Locate every malaria parasite.
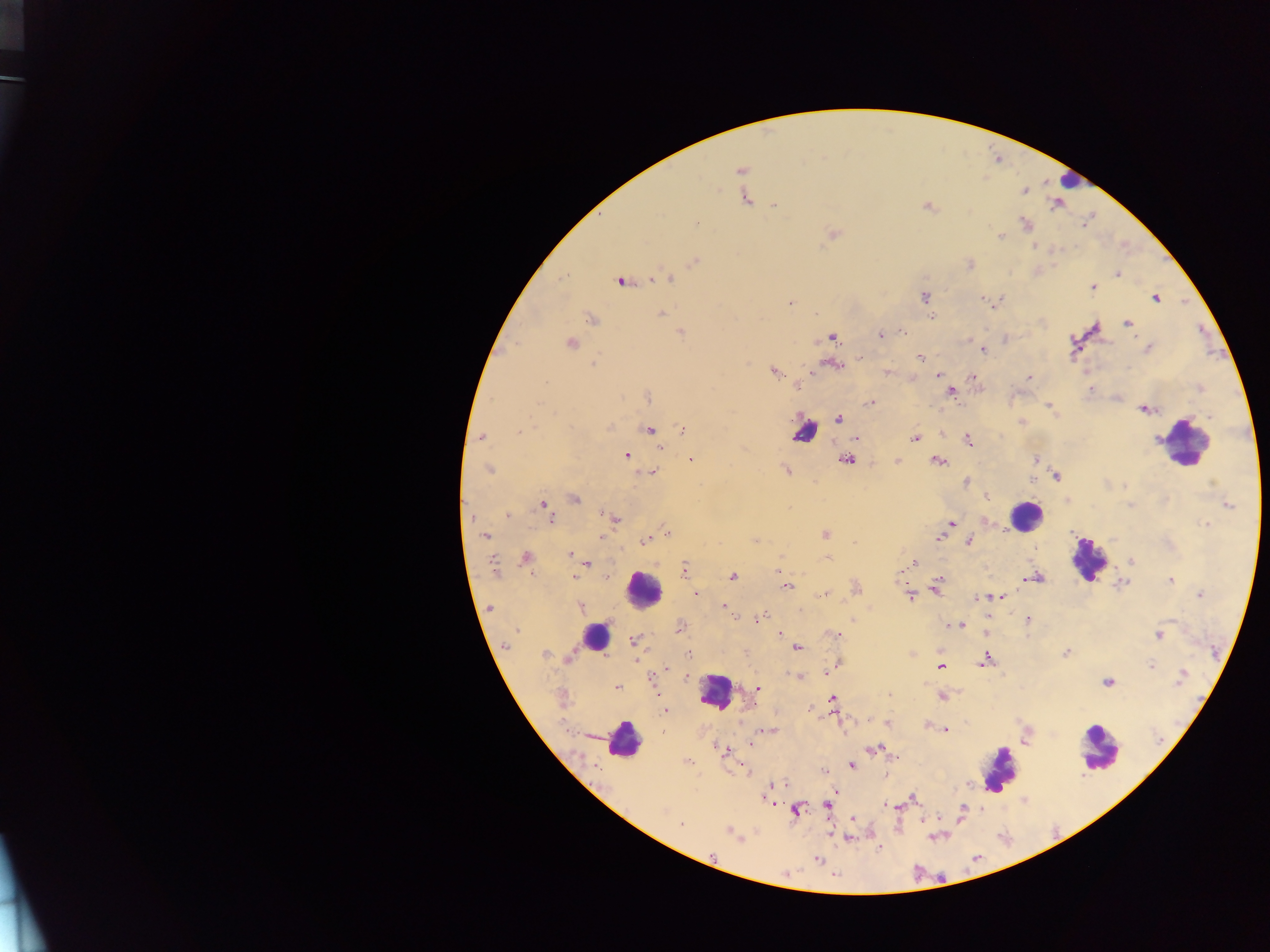
Approximate centers as [x, y] in pixels.
Malaria parasites: [741, 170], [1024, 191], [745, 199], [774, 205], [927, 206], [696, 224], [1025, 225], [833, 234], [1000, 236], [1035, 247], [694, 261], [970, 265], [1118, 275], [667, 278], [621, 281], [1092, 287], [925, 296], [1155, 298], [982, 299], [789, 303], [995, 303], [661, 313], [816, 315], [931, 317], [592, 319], [1127, 323], [681, 332], [901, 332], [881, 335], [833, 338], [572, 342], [1147, 348], [983, 351], [861, 357], [920, 357], [594, 364], [832, 365], [774, 372], [938, 374], [972, 375], [1029, 377], [545, 382], [1200, 388], [951, 392], [648, 397], [870, 403], [539, 404], [1049, 406], [1144, 409], [1210, 416], [839, 419], [1021, 422], [608, 428], [683, 429], [649, 430], [520, 432], [482, 437], [856, 438], [914, 438], [968, 440], [661, 447], [626, 456], [1035, 459], [846, 460], [692, 461], [897, 461], [938, 462], [489, 470], [786, 471], [653, 472], [1057, 477], [1032, 479], [966, 482], [987, 496], [575, 499], [543, 504], [1229, 505], [1130, 506], [508, 515], [551, 519], [614, 519], [951, 523], [1207, 525], [667, 531], [825, 534], [486, 536], [939, 538], [646, 540], [755, 540], [969, 542], [570, 555], [780, 557], [526, 558], [828, 558], [1131, 561], [587, 564], [911, 564], [493, 566], [684, 569], [901, 570], [733, 576], [573, 577], [606, 577], [783, 578], [1036, 578], [1170, 580], [1123, 583], [787, 586], [936, 589], [697, 594], [823, 595], [1200, 595], [910, 596], [995, 597], [1001, 597], [977, 598], [724, 605], [581, 607], [489, 608], [758, 618], [1027, 620], [953, 625], [960, 625], [680, 627], [780, 634], [837, 635], [1159, 635], [634, 641], [507, 644], [797, 647], [1066, 652], [688, 653], [545, 654], [569, 656], [986, 660], [837, 664], [1151, 665], [940, 667], [1182, 676], [686, 677], [798, 677], [1107, 683], [617, 687], [757, 688], [889, 696], [942, 697], [832, 699], [810, 709], [665, 710], [887, 723], [929, 727], [769, 730], [945, 730], [749, 744], [719, 749], [874, 749], [893, 756], [688, 762], [852, 765], [823, 771], [777, 784], [771, 788], [912, 799], [889, 805], [827, 806], [663, 810], [796, 810], [853, 819], [681, 825], [729, 831], [847, 838], [817, 859].

Leukocyte locations: [1068, 180], [803, 432], [1177, 441], [1025, 515], [1087, 559], [643, 589], [594, 636], [716, 692], [622, 741], [1098, 749], [999, 769]. Mobile-phone photograph taken through the microscope. Thick blood film. Image is 1270×952 pixels. Single field of view. Collected in Ghana.